Report the malaria status of this cell.
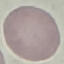

Uninfected.

Thin smear of blood. Giemsa stain. Automatically extracted cell patch, resized to 64 × 64 pixels. Photographed with a smartphone camera at the microscope eyepiece.